Name the blood parasite species.
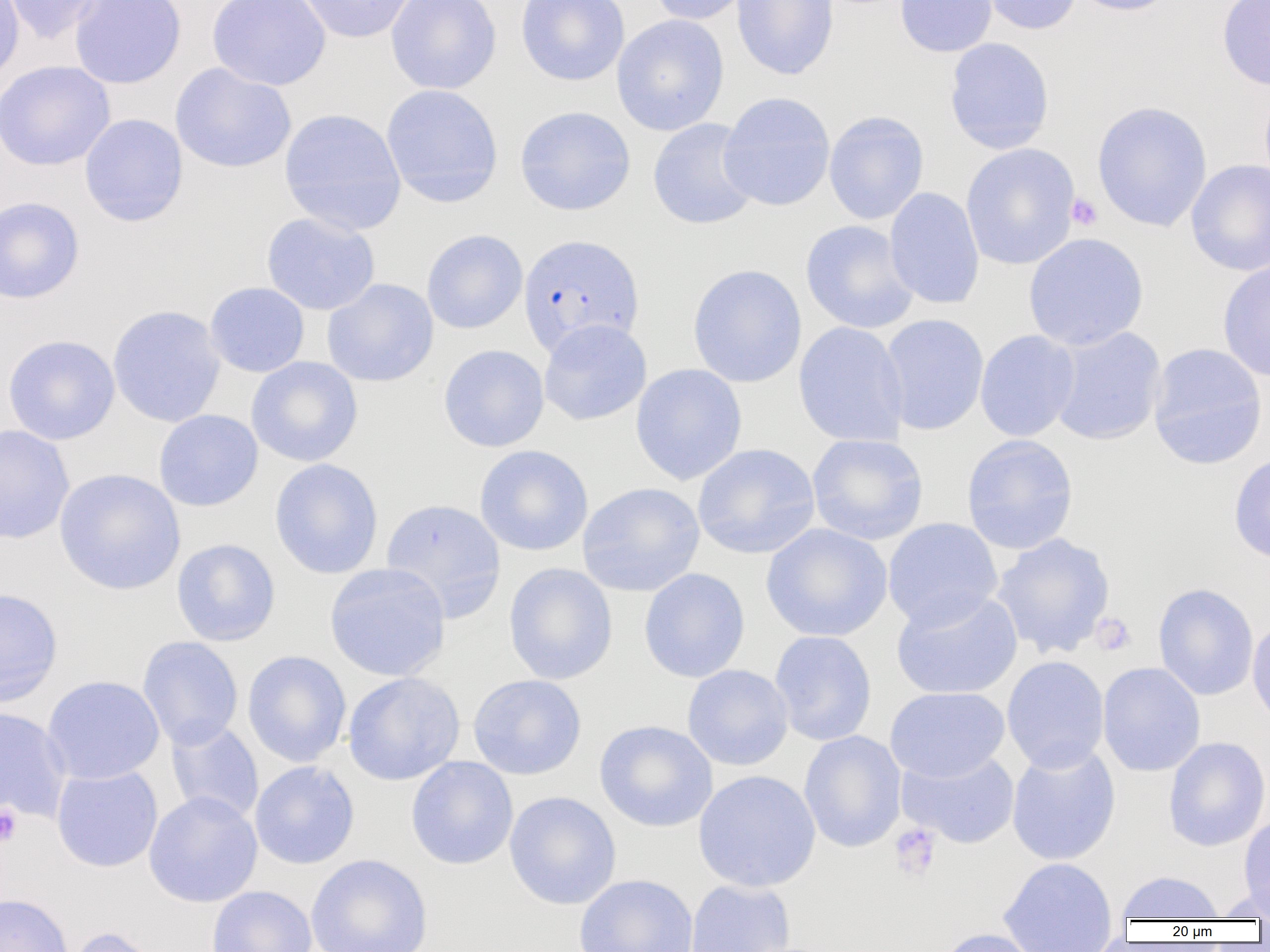
Plasmodium falciparum.

platelet locations = approximate bounding boxes as (x1, y1, x2, y2) in pixels: (1066, 193, 1103, 231), (1089, 612, 1136, 656), (0, 805, 22, 847), (889, 823, 941, 882)
modality = optical microscopy
Plasmodium falciparum-infected red blood cell locations = approximate bounding boxes as (x1, y1, x2, y2) in pixels: (518, 234, 645, 356)
image size = 1270×952 pixels
magnification = 1000x
preparation = thin blood smear
uninfected red blood cell locations = approximate bounding boxes as (x1, y1, x2, y2) in pixels: (0, 0, 25, 86), (2, 0, 104, 44), (69, 0, 187, 89), (207, 0, 330, 91), (296, 0, 417, 43), (386, 0, 501, 94), (515, 0, 630, 86), (646, 0, 755, 25), (731, 0, 839, 81), (895, 0, 997, 57), (979, 0, 1082, 35), (1069, 0, 1180, 16), (1216, 0, 1270, 90), (611, 14, 729, 136), (944, 37, 1054, 154), (0, 60, 115, 171), (170, 63, 297, 173), (381, 84, 503, 208), (718, 91, 836, 212), (1091, 100, 1212, 232), (515, 105, 636, 216), (279, 108, 407, 235), (823, 110, 929, 225), (79, 113, 188, 227), (647, 118, 760, 231), (960, 143, 1081, 271), (1186, 159, 1270, 276), (883, 187, 985, 310), (0, 196, 85, 304), (261, 212, 380, 315), (800, 219, 919, 334), (421, 229, 528, 334), (1023, 232, 1149, 351), (1217, 258, 1270, 382), (687, 264, 807, 388), (322, 278, 439, 387), (204, 282, 310, 377), (107, 305, 226, 428), (879, 314, 989, 435), (538, 319, 652, 426), (793, 321, 909, 448), (1047, 326, 1166, 446), (974, 330, 1080, 442), (2, 334, 120, 445), (1148, 342, 1268, 471), (438, 344, 550, 452), (246, 356, 363, 467), (630, 363, 747, 485), (153, 409, 263, 512), (0, 424, 74, 545), (806, 433, 929, 545), (961, 434, 1079, 555), (692, 443, 820, 559), (474, 445, 594, 556), (1228, 452, 1270, 564), (270, 458, 384, 579), (54, 468, 185, 596), (577, 482, 705, 597), (380, 498, 507, 622), (882, 517, 1003, 631), (761, 523, 893, 642), (991, 532, 1116, 659), (171, 538, 281, 646), (503, 562, 618, 685), (324, 563, 450, 682), (638, 567, 750, 683), (1153, 583, 1259, 701), (0, 587, 63, 707), (890, 589, 1023, 700), (1247, 617, 1270, 730), (769, 630, 877, 746), (137, 636, 243, 750), (242, 650, 352, 767), (1002, 656, 1110, 773), (1097, 661, 1206, 776), (682, 664, 794, 771), (343, 672, 465, 786), (468, 674, 587, 780), (41, 675, 165, 785), (884, 686, 1010, 782), (0, 705, 72, 823), (594, 720, 718, 833), (165, 721, 264, 825), (799, 730, 907, 853), (1163, 736, 1270, 852), (1006, 742, 1121, 867), (897, 749, 1020, 849), (406, 757, 518, 870), (249, 760, 360, 869), (51, 765, 163, 872), (693, 769, 821, 893), (143, 791, 263, 908), (504, 791, 622, 910), (1239, 813, 1270, 917), (306, 854, 433, 952), (997, 856, 1117, 952), (1116, 871, 1225, 921), (574, 874, 699, 952), (684, 879, 796, 952), (206, 885, 317, 952), (1210, 886, 1270, 921), (0, 892, 74, 952), (62, 925, 165, 952), (936, 928, 1045, 952)
field of view = one of a larger specimen